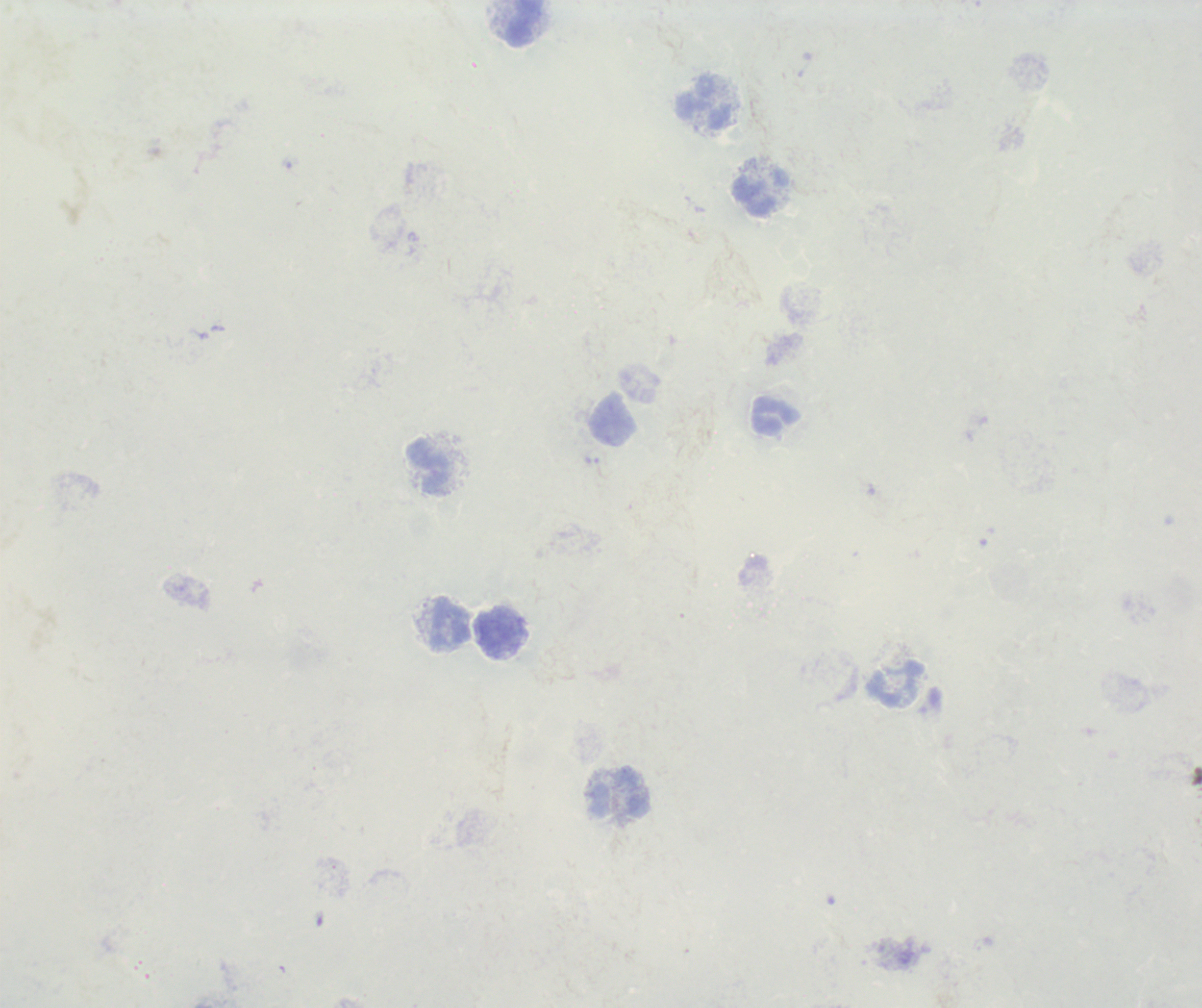 Approximate centers as (x, y) in pixels. Leukocyte locations: (525, 22), (703, 103), (759, 192), (775, 416), (614, 421), (430, 467), (451, 622), (502, 633), (896, 682), (619, 793). One field from this slide. Background quality: poor. 100x magnification. Thick blood film. Romanowsky stain. Result: no Plasmodium parasites seen. Previously used in an actual diagnosis. Image is 1202×1008 pixels.